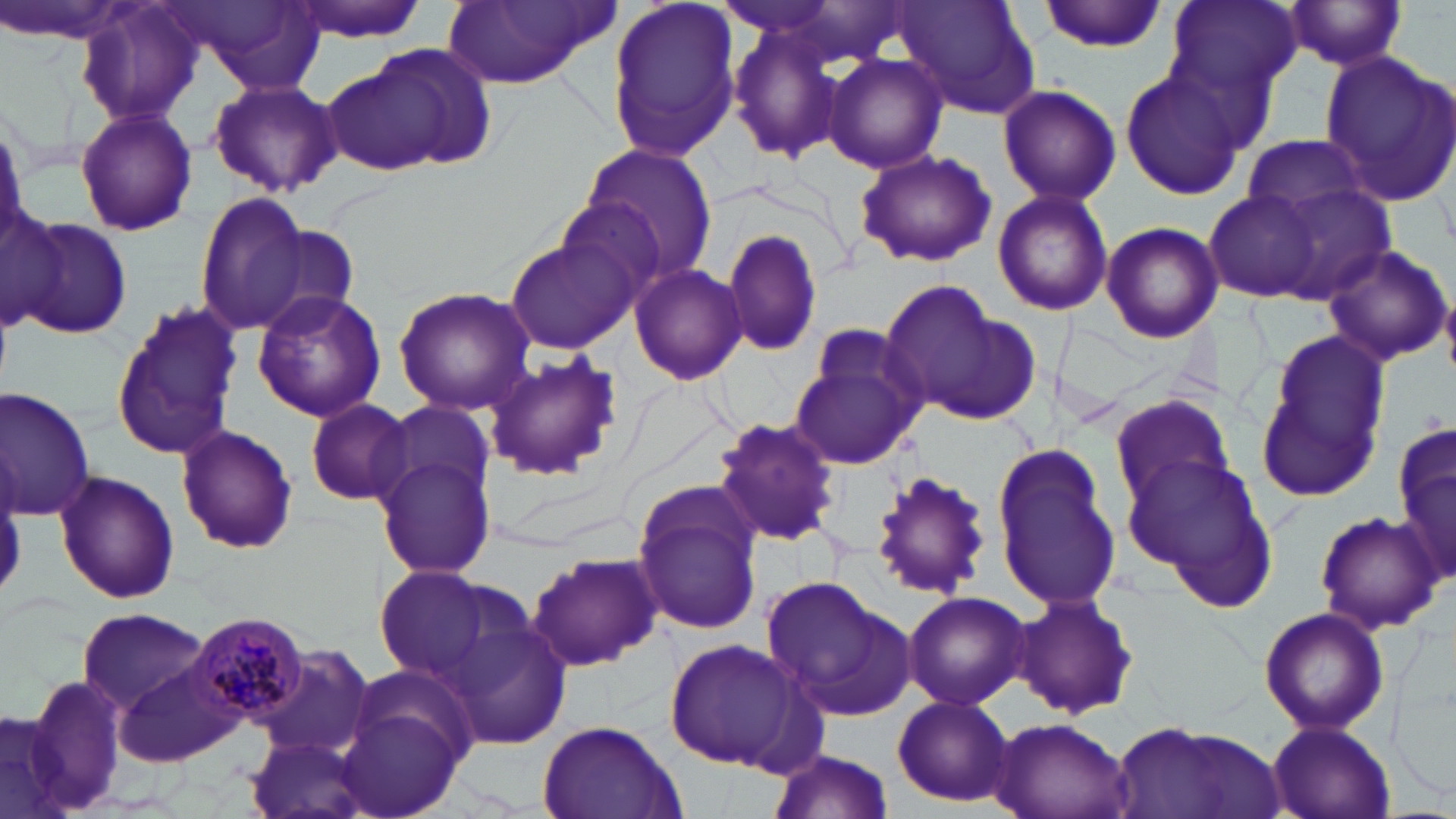
Summary:
  - Coordinate format: approximate bounding boxes as (x1, y1, x2, y2) in pixels
  - Uninfected red blood cell locations: (71, 0, 204, 127), (284, 0, 431, 41), (440, 0, 614, 89), (604, 0, 740, 166), (710, 0, 856, 41), (1162, 0, 1302, 104), (1283, 0, 1410, 73), (891, 1, 1040, 119), (1040, 1, 1169, 51), (177, 3, 328, 88), (724, 17, 846, 165), (357, 42, 498, 171), (1319, 49, 1456, 207), (823, 54, 950, 174), (321, 63, 444, 178), (1118, 66, 1249, 200), (208, 77, 342, 198), (996, 84, 1121, 206), (75, 105, 197, 237), (1242, 132, 1369, 220), (576, 144, 720, 286), (854, 149, 996, 268), (1269, 184, 1396, 303), (991, 186, 1114, 316), (1206, 189, 1324, 304), (192, 190, 309, 333), (0, 204, 65, 335), (13, 215, 134, 342), (1100, 221, 1223, 344), (245, 224, 361, 334), (720, 227, 824, 360), (504, 238, 634, 354), (1319, 242, 1453, 367), (629, 263, 747, 385), (877, 283, 1034, 425), (1441, 283, 1456, 377), (393, 287, 535, 414), (251, 290, 386, 422), (108, 303, 244, 461), (1252, 335, 1388, 504), (791, 337, 927, 468), (482, 352, 623, 482), (2, 387, 97, 522), (1108, 395, 1234, 517), (302, 401, 417, 507), (371, 401, 499, 507), (712, 415, 843, 546), (175, 424, 298, 557), (991, 445, 1125, 614), (374, 453, 497, 580), (1125, 453, 1274, 592), (1392, 453, 1456, 592), (867, 467, 994, 600), (52, 468, 181, 605), (632, 497, 764, 634), (1314, 510, 1445, 633), (527, 550, 662, 671), (370, 568, 499, 677), (762, 577, 915, 720), (903, 590, 1031, 712), (1012, 590, 1140, 722), (1257, 606, 1390, 735), (77, 607, 210, 713), (440, 608, 576, 751), (664, 636, 810, 772), (255, 648, 374, 760), (114, 660, 244, 767), (344, 660, 485, 781), (21, 672, 128, 816), (890, 694, 1016, 805), (0, 704, 75, 817), (338, 706, 465, 819), (988, 715, 1132, 819), (535, 719, 686, 819), (1105, 720, 1289, 819), (1267, 720, 1395, 819), (245, 733, 373, 819), (771, 748, 893, 819)
  - Plasmodium malariae-infected red blood cell locations: (184, 610, 311, 726)
  - Slide-level diagnosis: Plasmodium malariae
  - Field of view: one of a larger specimen
  - Stain: May-Grünwald-Giemsa
  - Image size: 1456×819 pixels
  - Magnification: 1000x
  - Preparation: thin blood smear
  - Modality: light microscopy